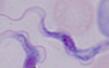
modality = micrograph
identification = trypanosome
magnification = 1000x